Locate every blood parasite and identify its species.
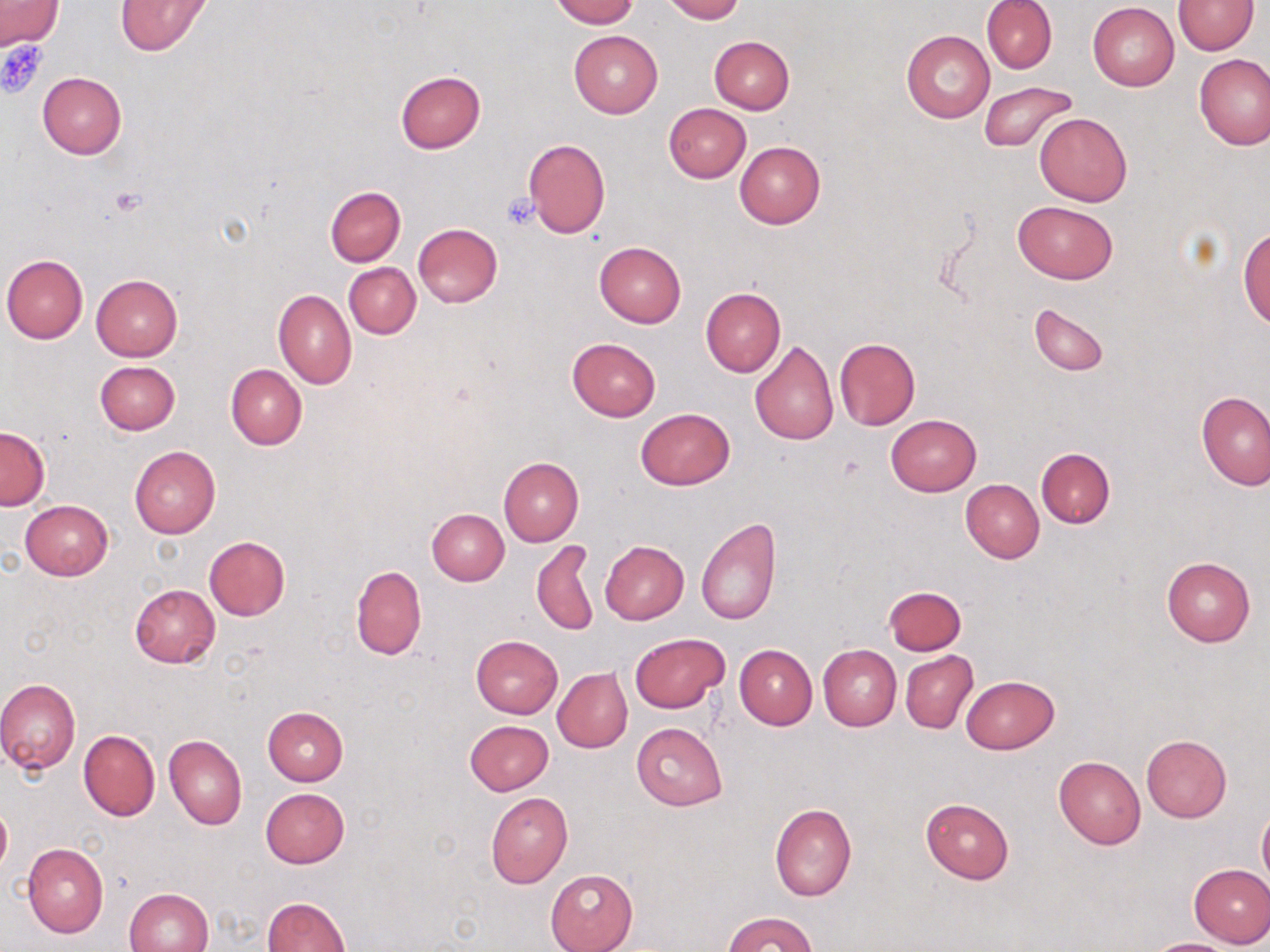
No blood parasites seen.

Summary:
  - Coordinate format: approximate bounding boxes as (x1, y1, x2, y2) in pixels
  - Uninfected red blood cell locations: (549, 0, 639, 27), (661, 0, 742, 22), (983, 0, 1057, 73), (1, 1, 63, 49), (113, 1, 212, 57), (1172, 1, 1258, 55), (1087, 2, 1179, 91), (902, 30, 995, 123), (569, 31, 662, 118), (709, 36, 794, 114), (1194, 53, 1270, 149), (396, 71, 485, 153), (37, 72, 126, 159), (979, 79, 1079, 153), (663, 103, 751, 183), (1035, 111, 1132, 205), (523, 139, 610, 237), (735, 142, 826, 229), (324, 186, 405, 267), (1013, 201, 1119, 283), (412, 224, 502, 308), (1239, 227, 1270, 328), (594, 241, 686, 327), (1, 254, 89, 343), (344, 262, 420, 339), (91, 274, 183, 362), (700, 287, 786, 376), (273, 289, 356, 388), (1029, 303, 1109, 376), (567, 337, 661, 421), (835, 338, 920, 430), (749, 340, 839, 445), (95, 361, 180, 435), (225, 365, 306, 449), (1196, 391, 1270, 490), (636, 408, 734, 490), (886, 414, 981, 496), (0, 426, 51, 509), (130, 446, 220, 538), (1036, 447, 1115, 528), (498, 458, 584, 546), (961, 479, 1044, 562), (21, 499, 112, 579), (425, 508, 510, 585), (695, 517, 781, 627), (204, 535, 290, 620), (530, 539, 599, 636), (600, 540, 689, 624), (1162, 556, 1255, 645), (351, 565, 427, 660), (128, 584, 220, 667), (884, 585, 966, 655), (630, 631, 729, 713), (472, 635, 563, 718), (734, 645, 817, 730), (819, 645, 901, 730), (901, 651, 977, 733), (553, 667, 632, 753), (962, 676, 1059, 754), (0, 677, 80, 775), (262, 706, 348, 785), (465, 720, 554, 795), (631, 722, 727, 811), (78, 729, 159, 822), (164, 734, 246, 830), (1141, 734, 1231, 822), (1053, 755, 1146, 849), (260, 788, 350, 867), (486, 792, 572, 888), (921, 798, 1014, 883), (0, 801, 11, 879), (1257, 803, 1270, 891), (769, 804, 857, 901), (23, 843, 107, 939), (1188, 863, 1270, 948), (544, 870, 638, 952), (125, 888, 215, 952), (262, 897, 350, 951), (721, 912, 820, 952), (1143, 939, 1240, 952)
  - Platelet locations: (0, 39, 49, 98), (108, 187, 148, 218), (500, 192, 544, 231)
  - Slide-level diagnosis: no evidence of blood parasites
  - Image size: 1270×952 pixels
  - Field of view: one of a larger specimen
  - Magnification: 1000x
  - Modality: light microscopy
  - Preparation: thin blood smear
  - Stain: May-Grünwald-Giemsa